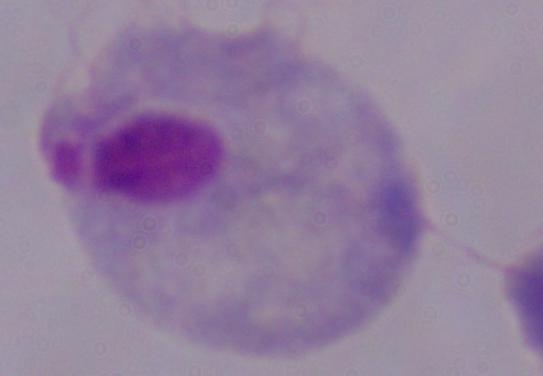

Summary:
  - Modality: photomicrograph
  - Magnification: 1000x
  - Identification: trichomonad